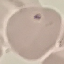

malaria status = uninfected
image type = cell patch, automatically extracted from a larger field of view and resized to 64 × 64 pixels
stain = Giemsa
capture = smartphone through the microscope eyepiece
preparation = thin smear